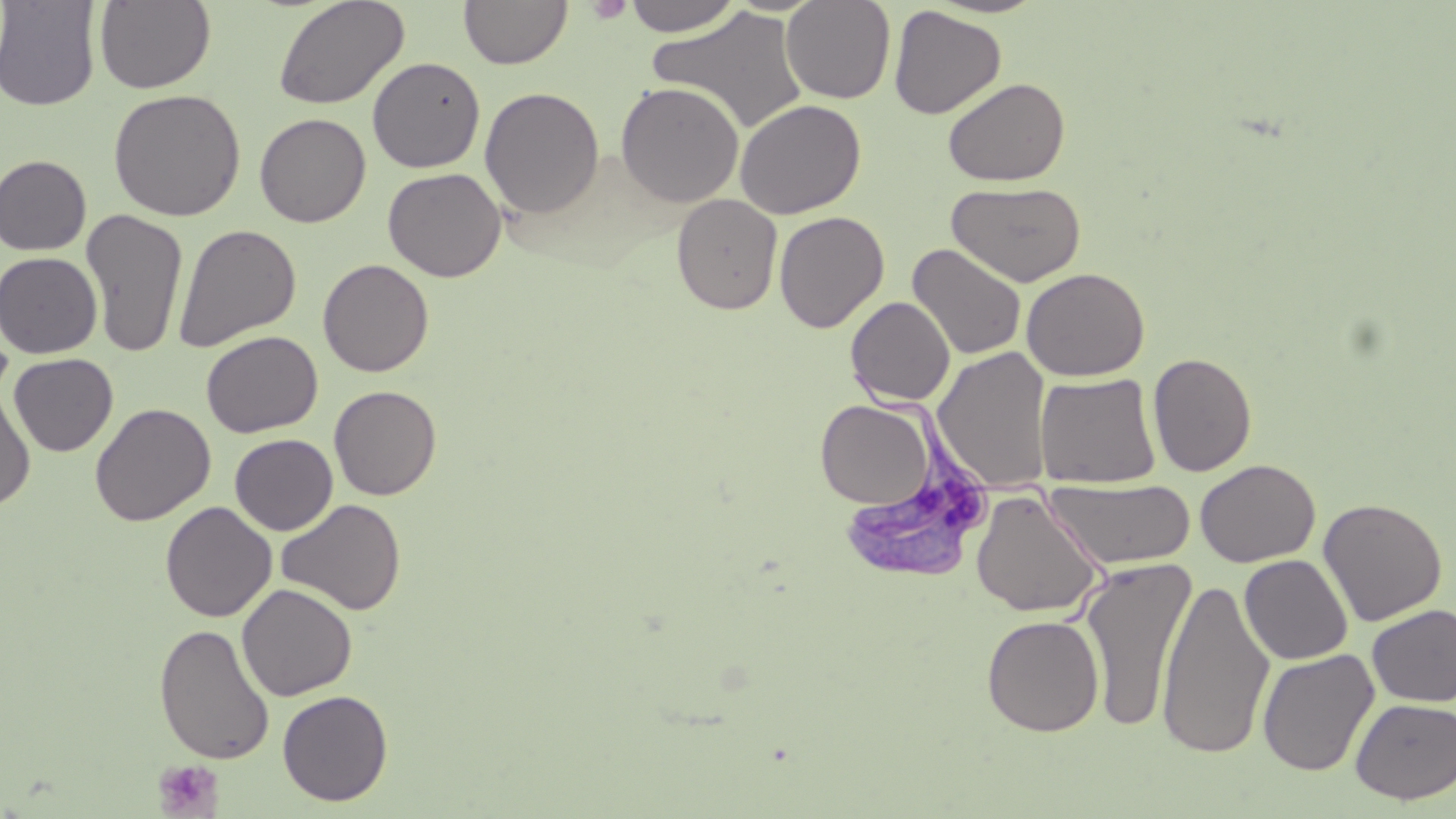
slide-level diagnosis = Trypanosoma brucei
preparation = thin blood smear
Trypanosoma brucei locations = approximate bounding boxes as (x1, y1, x2, y2) in pixels: (846, 360, 995, 584)
platelet locations = approximate bounding boxes as (x1, y1, x2, y2) in pixels: (585, 0, 633, 23), (153, 759, 225, 818)
modality = light microscopy
magnification = 1000x
stain = May-Grünwald-Giemsa
uninfected red blood cell locations = approximate bounding boxes as (x1, y1, x2, y2) in pixels: (0, 0, 102, 112), (94, 0, 216, 93), (273, 0, 409, 111), (459, 0, 572, 70), (622, 0, 744, 36), (780, 0, 896, 104), (888, 5, 1006, 119), (648, 7, 809, 135), (367, 56, 485, 173), (943, 77, 1070, 187), (615, 81, 744, 208), (480, 87, 605, 219), (108, 89, 246, 221), (734, 99, 866, 219), (254, 113, 371, 227), (0, 155, 92, 256), (382, 167, 506, 282), (946, 181, 1087, 288), (671, 193, 783, 314), (80, 209, 189, 358), (774, 210, 889, 332), (173, 223, 301, 351), (907, 243, 1027, 361), (0, 252, 102, 357), (318, 259, 434, 377), (1021, 267, 1150, 381), (846, 296, 955, 405), (201, 331, 323, 437), (933, 346, 1053, 493), (9, 353, 118, 456), (1148, 353, 1257, 477), (1035, 373, 1161, 488), (329, 385, 442, 500), (0, 387, 36, 510), (815, 400, 936, 509), (90, 403, 215, 526), (229, 434, 338, 535), (1195, 459, 1320, 568), (1045, 478, 1196, 571), (971, 490, 1105, 618), (1318, 497, 1448, 626), (276, 498, 406, 616), (160, 501, 276, 622), (1240, 554, 1353, 664), (1079, 557, 1196, 734), (1157, 576, 1274, 760), (236, 583, 358, 701), (1366, 604, 1456, 706), (981, 614, 1104, 737), (154, 623, 275, 765), (1256, 648, 1379, 776), (277, 689, 393, 806), (1350, 698, 1456, 804)
field of view = one of a larger specimen
image size = 1456×819 pixels